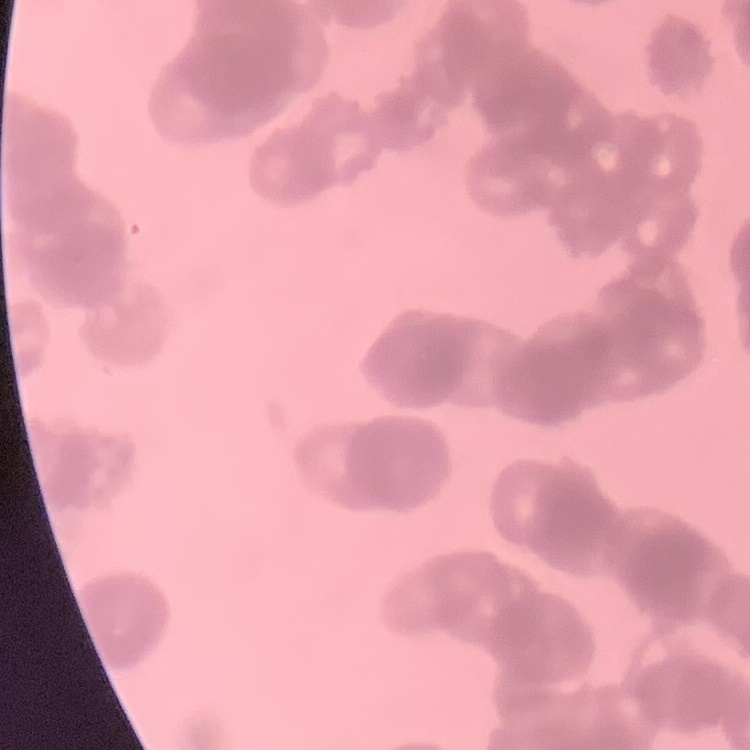

Summary:
  - Erythrocyte morphology: rouleaux formation
  - Stain: Field's or Giemsa
  - Image type: one tile cut from a larger photomicrograph
  - Preparation: thin blood film